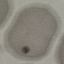
result = no malaria parasites detected
preparation = thin smear
stain = Giemsa
image type = cell patch, automatically extracted from a larger field of view and resized to 64 × 64 pixels
capture = smartphone through the microscope eyepiece